Name the blood parasite species.
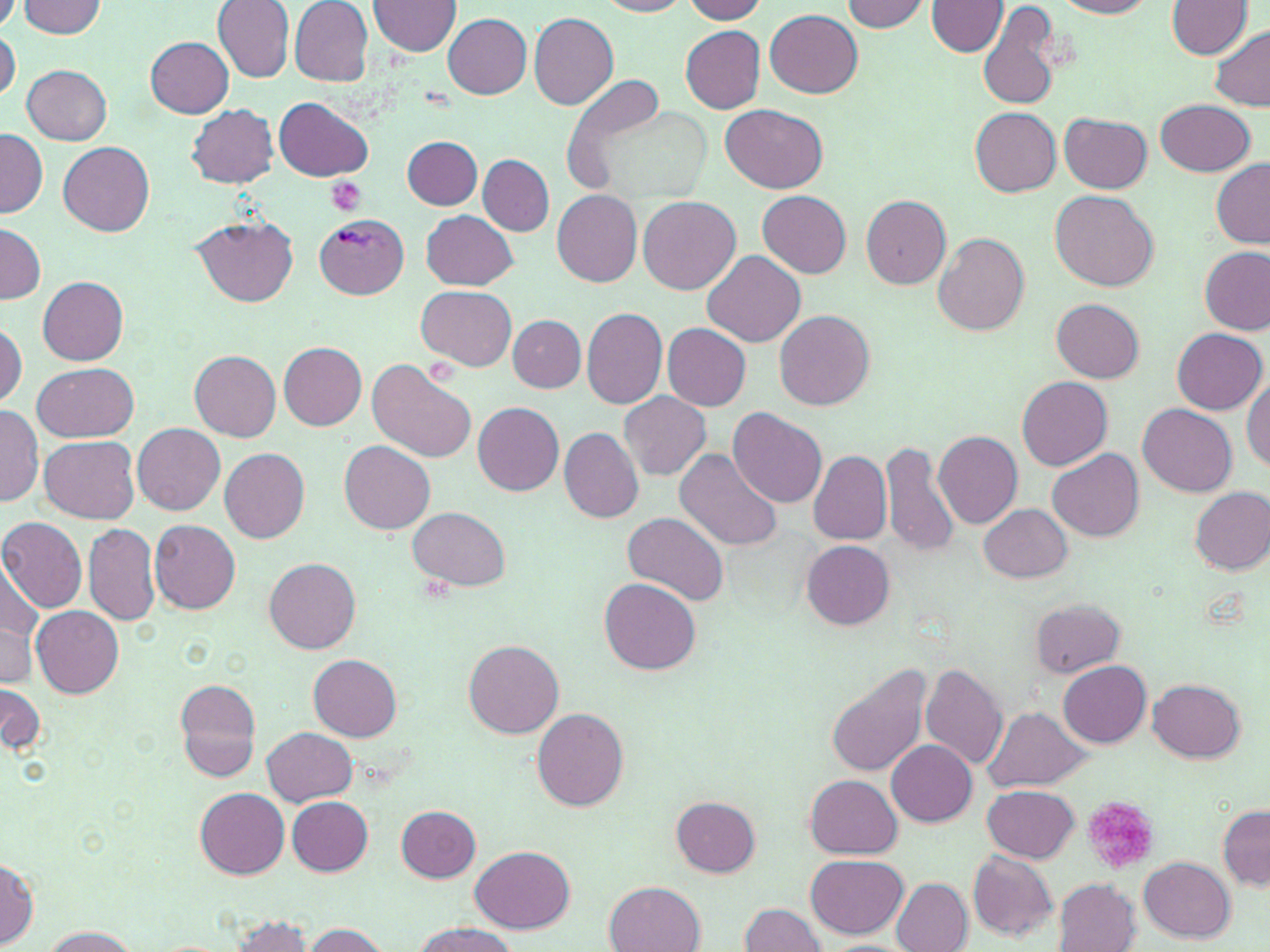
Plasmodium vivax.

Summary:
  - Coordinate format: approximate bounding boxes as [x1, y1, x2, y2] in pixels
  - Plasmodium vivax-infected red blood cell locations: [315, 214, 410, 298]
  - Uninfected red blood cell locations: [211, 0, 296, 82], [371, 0, 463, 56], [597, 0, 692, 17], [681, 0, 769, 22], [1055, 0, 1157, 17], [18, 1, 107, 36], [289, 1, 373, 84], [842, 1, 929, 32], [928, 1, 1008, 56], [979, 1, 1064, 112], [1168, 1, 1255, 58], [766, 9, 862, 98], [528, 12, 620, 109], [443, 14, 532, 99], [681, 26, 766, 114], [1207, 26, 1270, 112], [1, 27, 20, 104], [147, 37, 235, 117], [22, 65, 113, 144], [274, 96, 373, 182], [1155, 98, 1256, 177], [722, 103, 828, 193], [185, 104, 279, 188], [969, 107, 1062, 195], [1060, 114, 1151, 193], [1, 128, 47, 218], [403, 135, 482, 209], [59, 141, 155, 234], [479, 155, 554, 235], [1210, 157, 1270, 247], [552, 189, 643, 287], [757, 190, 851, 276], [1050, 190, 1158, 293], [861, 195, 951, 289], [639, 197, 740, 293], [422, 210, 517, 290], [191, 215, 299, 307], [1, 222, 44, 305], [932, 233, 1029, 337], [1200, 246, 1268, 335], [702, 249, 805, 347], [39, 278, 129, 364], [417, 284, 517, 368], [1052, 298, 1145, 382], [582, 308, 668, 407], [774, 309, 875, 409], [509, 315, 586, 391], [0, 320, 28, 410], [663, 324, 752, 411], [1172, 327, 1267, 414], [279, 342, 367, 430], [189, 350, 282, 439], [366, 358, 477, 465], [33, 362, 137, 443], [1017, 376, 1112, 470], [1242, 377, 1270, 472], [617, 391, 711, 480], [473, 402, 564, 496], [1138, 403, 1237, 496], [0, 406, 42, 504], [728, 407, 826, 507], [133, 424, 225, 514], [559, 427, 645, 521], [934, 430, 1022, 530], [39, 437, 139, 522], [881, 438, 960, 559], [339, 441, 434, 534], [219, 447, 310, 544], [674, 449, 781, 552], [1047, 449, 1144, 540], [807, 450, 891, 545], [1192, 488, 1270, 574], [979, 505, 1072, 582], [408, 507, 509, 590], [623, 512, 729, 607], [0, 516, 88, 614], [148, 519, 241, 614], [84, 521, 160, 627], [800, 539, 894, 630], [265, 557, 360, 654], [0, 564, 42, 674], [599, 579, 701, 674], [1032, 600, 1126, 676], [31, 606, 123, 698], [0, 625, 36, 688], [463, 639, 563, 738], [309, 654, 403, 739], [1059, 661, 1152, 748], [828, 664, 932, 779], [919, 664, 1008, 771], [1148, 678, 1244, 762], [177, 679, 260, 781], [0, 680, 46, 758], [531, 708, 629, 810], [985, 708, 1087, 789], [263, 727, 357, 806], [886, 740, 977, 827], [805, 774, 901, 857], [982, 786, 1080, 863], [197, 789, 289, 878], [286, 797, 374, 875], [671, 797, 760, 877], [396, 805, 482, 881], [1218, 805, 1268, 891], [473, 846, 574, 932], [966, 851, 1058, 942], [805, 853, 908, 939], [1, 855, 40, 947], [1137, 856, 1236, 942], [892, 878, 972, 952], [1055, 879, 1141, 952], [604, 881, 705, 952], [738, 901, 829, 952], [224, 916, 316, 951], [410, 920, 518, 952], [300, 923, 391, 952], [40, 926, 139, 951]
  - Platelet locations: [325, 177, 367, 216], [1081, 796, 1160, 873]
  - Preparation: thin blood film
  - Magnification: 1000x
  - Modality: light microscopy
  - Field of view: single
  - Stain: May-Grünwald-Giemsa
  - Image size: 1270×952 pixels